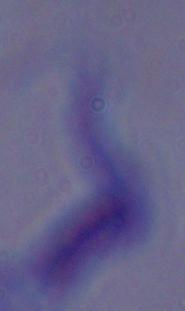 A trypanosome is seen. 1000x magnification. Photomicrograph.